Classify this cell by malaria status.
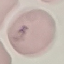
Parasitized.

Summary:
  - Capture: smartphone camera at the microscope eyepiece
  - Image type: cell patch, automatically extracted from a larger field of view and resized to 64 × 64 pixels
  - Stain: Giemsa
  - Preparation: thin smear